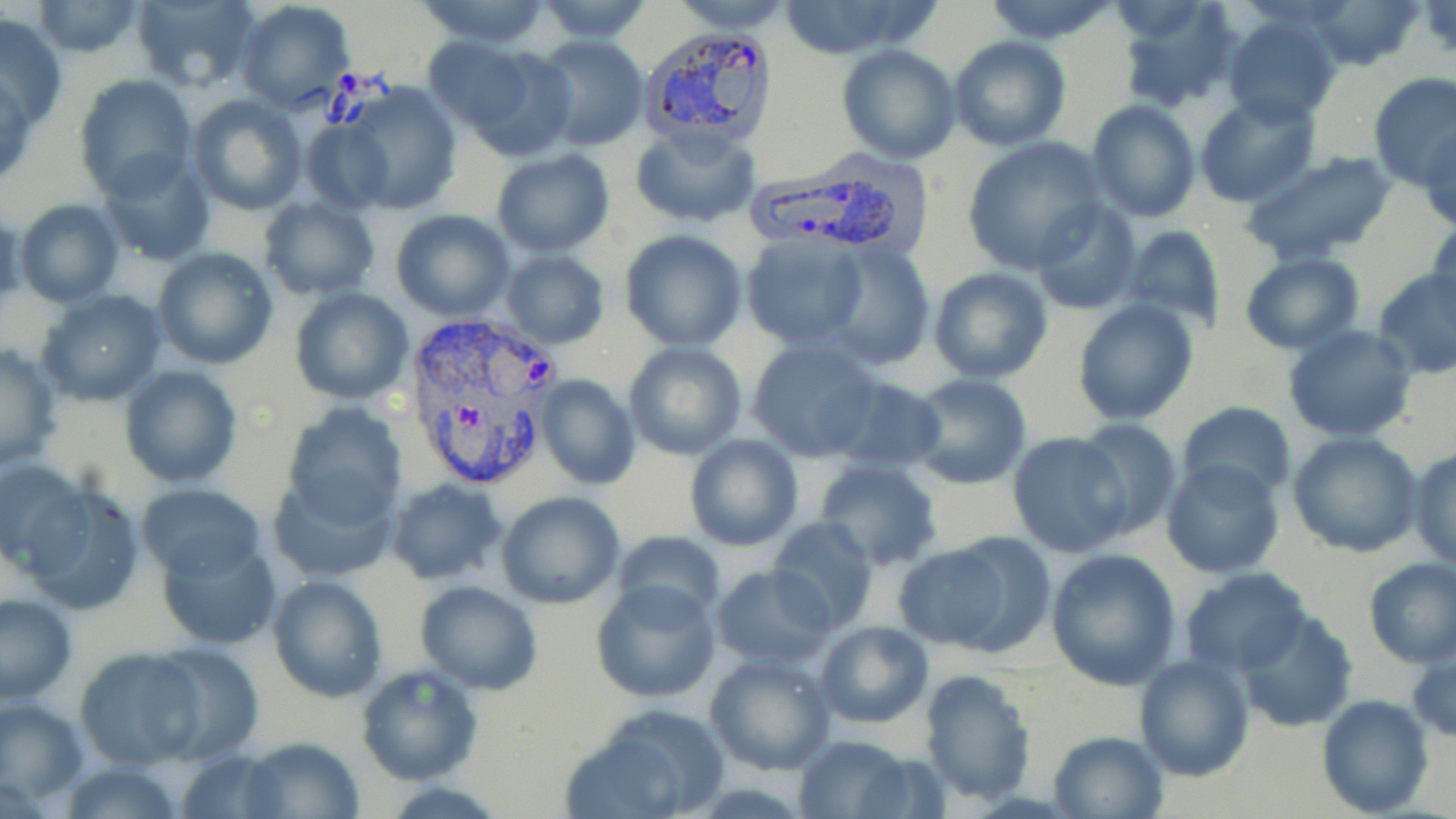 Approximate bounding boxes as named x1/y1/x2/y2 corners in pixels. Plasmodium vivax-infected red blood cell locations: (x1=638, y1=25, x2=778, y2=153), (x1=747, y1=157, x2=926, y2=257), (x1=400, y1=312, x2=556, y2=495). Uninfected red blood cell locations: (x1=130, y1=0, x2=262, y2=92), (x1=415, y1=0, x2=555, y2=47), (x1=666, y1=0, x2=797, y2=33), (x1=981, y1=0, x2=1122, y2=44), (x1=1114, y1=0, x2=1244, y2=113), (x1=1309, y1=0, x2=1423, y2=71), (x1=33, y1=1, x2=145, y2=57), (x1=234, y1=1, x2=356, y2=112), (x1=534, y1=1, x2=654, y2=45), (x1=770, y1=1, x2=940, y2=60), (x1=1, y1=11, x2=67, y2=130), (x1=1221, y1=14, x2=1341, y2=125), (x1=949, y1=35, x2=1070, y2=151), (x1=533, y1=36, x2=649, y2=152), (x1=422, y1=38, x2=534, y2=134), (x1=836, y1=44, x2=962, y2=165), (x1=459, y1=46, x2=578, y2=161), (x1=1367, y1=71, x2=1456, y2=192), (x1=76, y1=75, x2=197, y2=197), (x1=341, y1=85, x2=463, y2=213), (x1=1194, y1=91, x2=1320, y2=205), (x1=187, y1=93, x2=306, y2=216), (x1=1084, y1=99, x2=1200, y2=222), (x1=300, y1=119, x2=395, y2=215), (x1=631, y1=123, x2=759, y2=230), (x1=1421, y1=123, x2=1456, y2=234), (x1=961, y1=137, x2=1106, y2=271), (x1=1238, y1=148, x2=1403, y2=265), (x1=96, y1=150, x2=216, y2=265), (x1=491, y1=150, x2=616, y2=257), (x1=260, y1=197, x2=380, y2=300), (x1=1029, y1=199, x2=1140, y2=314), (x1=15, y1=200, x2=123, y2=307), (x1=985, y1=204, x2=1117, y2=346), (x1=391, y1=208, x2=516, y2=321), (x1=1429, y1=211, x2=1456, y2=318), (x1=1122, y1=224, x2=1226, y2=330), (x1=618, y1=229, x2=748, y2=351), (x1=740, y1=232, x2=870, y2=349), (x1=823, y1=242, x2=935, y2=370), (x1=152, y1=247, x2=278, y2=369), (x1=501, y1=251, x2=609, y2=347), (x1=1239, y1=253, x2=1365, y2=354), (x1=928, y1=267, x2=1053, y2=384), (x1=1372, y1=268, x2=1456, y2=379), (x1=291, y1=287, x2=413, y2=405), (x1=37, y1=289, x2=167, y2=404), (x1=1073, y1=297, x2=1199, y2=425), (x1=1282, y1=325, x2=1419, y2=443), (x1=746, y1=337, x2=884, y2=462), (x1=0, y1=341, x2=63, y2=472), (x1=621, y1=341, x2=747, y2=460), (x1=117, y1=364, x2=242, y2=488), (x1=906, y1=374, x2=1033, y2=489), (x1=534, y1=376, x2=639, y2=490), (x1=827, y1=376, x2=947, y2=475), (x1=281, y1=401, x2=406, y2=524), (x1=1176, y1=401, x2=1295, y2=505), (x1=1072, y1=417, x2=1183, y2=541), (x1=1007, y1=431, x2=1133, y2=558), (x1=1287, y1=431, x2=1424, y2=557), (x1=684, y1=432, x2=802, y2=550), (x1=602, y1=442, x2=704, y2=547), (x1=1410, y1=446, x2=1456, y2=570), (x1=0, y1=457, x2=90, y2=578), (x1=812, y1=458, x2=944, y2=570), (x1=1161, y1=458, x2=1285, y2=579), (x1=913, y1=461, x2=1028, y2=555), (x1=267, y1=468, x2=403, y2=584), (x1=12, y1=475, x2=147, y2=613), (x1=385, y1=477, x2=508, y2=584), (x1=136, y1=484, x2=267, y2=579), (x1=496, y1=491, x2=624, y2=607), (x1=766, y1=517, x2=880, y2=634), (x1=614, y1=528, x2=725, y2=621), (x1=893, y1=534, x2=1049, y2=658), (x1=158, y1=537, x2=281, y2=649), (x1=1046, y1=548, x2=1183, y2=689), (x1=1362, y1=558, x2=1456, y2=669), (x1=711, y1=564, x2=836, y2=670), (x1=1179, y1=567, x2=1312, y2=678), (x1=266, y1=574, x2=387, y2=701), (x1=416, y1=579, x2=543, y2=694), (x1=591, y1=580, x2=720, y2=703), (x1=1, y1=594, x2=76, y2=705), (x1=1234, y1=610, x2=1356, y2=732), (x1=815, y1=621, x2=934, y2=729), (x1=150, y1=641, x2=264, y2=765), (x1=1408, y1=641, x2=1455, y2=743), (x1=75, y1=647, x2=200, y2=768), (x1=704, y1=650, x2=838, y2=775), (x1=1134, y1=654, x2=1254, y2=778), (x1=356, y1=662, x2=483, y2=785), (x1=919, y1=669, x2=1037, y2=805), (x1=1317, y1=694, x2=1433, y2=817), (x1=0, y1=696, x2=88, y2=806), (x1=565, y1=704, x2=731, y2=819), (x1=1048, y1=729, x2=1167, y2=817), (x1=793, y1=732, x2=919, y2=816), (x1=240, y1=736, x2=363, y2=818), (x1=179, y1=748, x2=290, y2=818), (x1=57, y1=761, x2=188, y2=819). Slide-level diagnosis: Plasmodium vivax. Captured at 1000x magnification. Image is 1456×819 pixels. Light microscopy. One field of a larger specimen. Thin blood film. May-Grünwald-Giemsa-stained preparation.